Assess this cell for malaria.
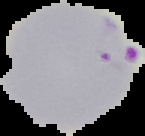

It is parasitized.

preparation = thin blood smear
image size = 145×136 pixels
image type = segmented cell region with the area outside set to black